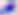

400x magnification. Photomicrograph. Toxoplasma gondii is shown.